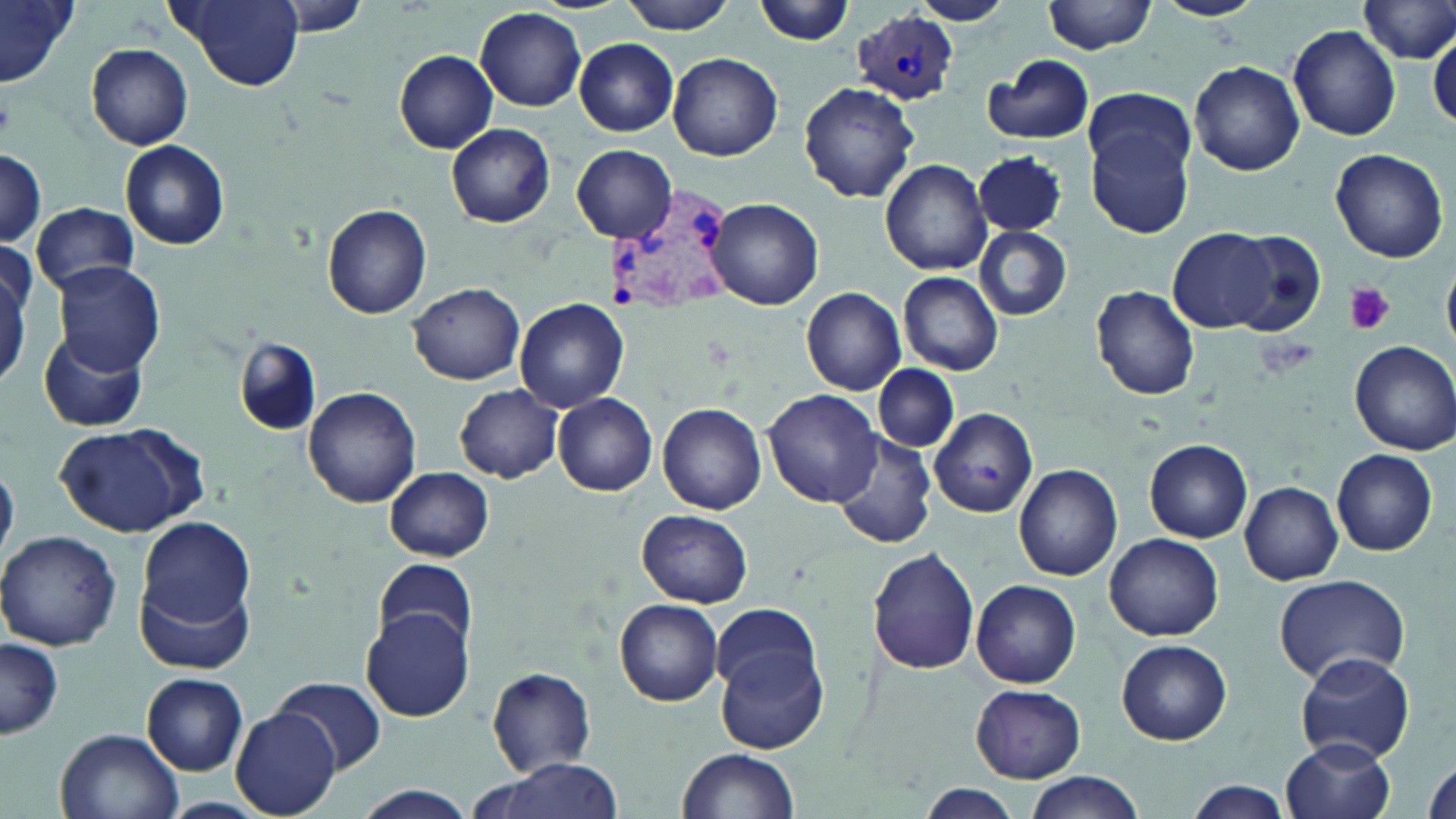
Plasmodium vivax-infected red blood cell locations = approximate bounding boxes as (x1,y1)-(x2,y2) corner pairs in pixels: (853,9)-(958,105), (601,180)-(742,318)
slide-level diagnosis = Plasmodium vivax
stain = May-Grünwald-Giemsa
field of view = one of a larger specimen
preparation = thin blood film
uninfected red blood cell locations = approximate bounding boxes as (x1,y1)-(x2,y2) corner pairs in pixels: (0,0)-(82,88), (166,0)-(305,91), (264,0)-(377,35), (616,0)-(737,34), (753,0)-(858,45), (1045,0)-(1158,53), (1155,0)-(1264,21), (913,1)-(1012,27), (1356,2)-(1456,65), (476,8)-(587,110), (1287,26)-(1401,139), (1428,27)-(1456,129), (573,39)-(680,135), (87,43)-(193,149), (395,51)-(498,153), (669,53)-(783,162), (985,55)-(1096,144), (1188,60)-(1304,175), (798,81)-(921,204), (1083,87)-(1196,178), (1086,121)-(1194,239), (447,124)-(555,228), (121,140)-(229,250), (573,146)-(676,243), (1331,147)-(1448,263), (0,150)-(47,249), (974,150)-(1068,237), (880,158)-(993,275), (705,198)-(824,311), (31,201)-(139,293), (321,205)-(431,319), (974,226)-(1071,320), (1169,226)-(1280,333), (1227,230)-(1329,339), (52,262)-(165,373), (0,268)-(29,387), (899,272)-(1003,376), (409,283)-(526,384), (1089,286)-(1202,399), (802,287)-(906,394), (515,298)-(629,411), (36,326)-(149,433), (235,337)-(320,436), (1350,339)-(1456,455), (874,364)-(958,452), (456,385)-(562,484), (302,386)-(422,509), (764,389)-(882,506), (553,393)-(658,495), (657,402)-(768,514), (931,406)-(1039,516), (55,424)-(207,538), (831,432)-(938,551), (1146,439)-(1253,542), (1332,449)-(1438,556), (0,460)-(19,566), (1015,465)-(1122,581), (386,466)-(495,562), (1240,482)-(1343,584), (636,509)-(753,608), (138,517)-(255,629), (0,530)-(122,651), (1104,533)-(1223,640), (867,547)-(980,676), (371,557)-(478,656), (135,573)-(255,675), (1273,573)-(1413,685), (970,579)-(1082,689), (615,599)-(723,706), (711,603)-(822,707), (361,609)-(473,722), (1,637)-(64,740), (1116,638)-(1231,745), (716,641)-(830,756), (1294,651)-(1416,765), (488,668)-(597,775), (142,673)-(249,775), (271,676)-(387,774), (970,684)-(1086,782), (230,709)-(340,816), (56,728)-(183,819), (1282,738)-(1396,819), (677,749)-(799,818), (1421,752)-(1456,819), (474,762)-(633,819), (1022,774)-(1147,819), (1183,780)-(1293,818), (916,783)-(1023,818), (348,787)-(483,819)
magnification = 1000x
modality = optical microscopy
platelet locations = approximate bounding boxes as (x1,y1)-(x2,y2) corner pairs in pixels: (1344,283)-(1394,336)
image size = 1456×819 pixels